Locate every Plasmodium parasite.
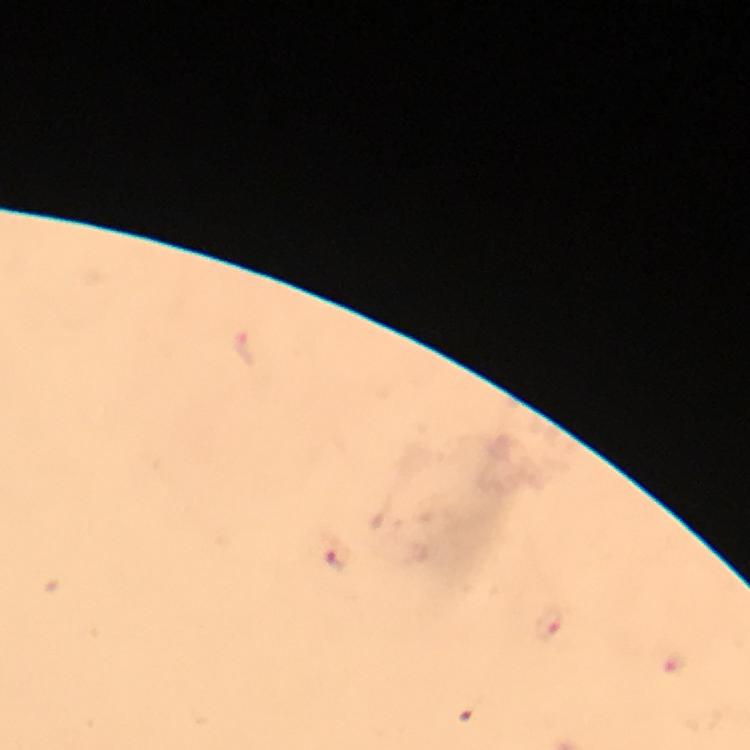

Approximate centers as {x, y} in pixels.
Plasmodium parasites: {337, 554}, {549, 624}.

Giemsa stain. From a diagnostic examination for malaria. 100x magnification. Immersion oil applied. Image is 750×750 pixels. Cropped region of a single field of view. Thick blood smear. Photographed with a smartphone mounted on the microscope.